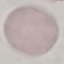
Result: no malaria parasites detected. Automatically extracted cell patch, resized to 64 × 64 pixels. Giemsa stain. Photographed with a smartphone camera at the microscope eyepiece. Thin blood film.